Classify this cell by malaria status.
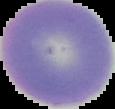
It is uninfected.

Summary:
  - Image type: segmented cell region on a black background
  - Preparation: thin blood smear
  - Image size: 115×109 pixels